Name the parasite shown.
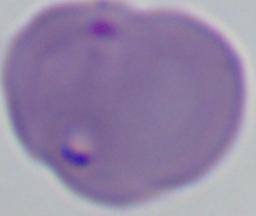

This is Babesia.

modality: photomicrograph
magnification: 1000x